Name the cell type shown.
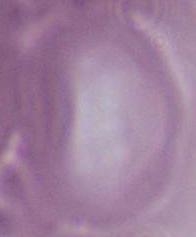
An erythrocyte.

Summary:
  - Modality: photomicrograph
  - Magnification: 1000x